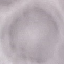
Summary:
  - Malaria status: uninfected
  - Image type: automatically extracted cell patch, resized to 64 × 64 pixels
  - Stain: Giemsa
  - Preparation: thin blood film
  - Capture: smartphone through the microscope eyepiece